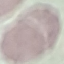

Summary:
  - Result: no malaria parasites detected
  - Preparation: thin blood film
  - Stain: Giemsa
  - Capture: smartphone camera at the microscope eyepiece
  - Image type: automatically extracted cell patch, resized to 64 × 64 pixels